Name the parasite shown.
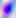
This is Toxoplasma gondii.

Captured at 400x magnification. Photomicrograph.